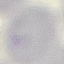

Summary:
  - Malaria status: uninfected
  - Capture: smartphone camera at the microscope eyepiece
  - Stain: Giemsa
  - Image type: automatically extracted cell patch, resized to 64 × 64 pixels
  - Preparation: thin smear